Report the malaria status of this cell.
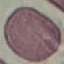
Uninfected.

{
  "preparation": "thin blood smear",
  "capture": "smartphone through the microscope eyepiece",
  "stain": "Giemsa",
  "image_type": "automatically extracted cell patch, resized to 64 × 64 pixels"
}